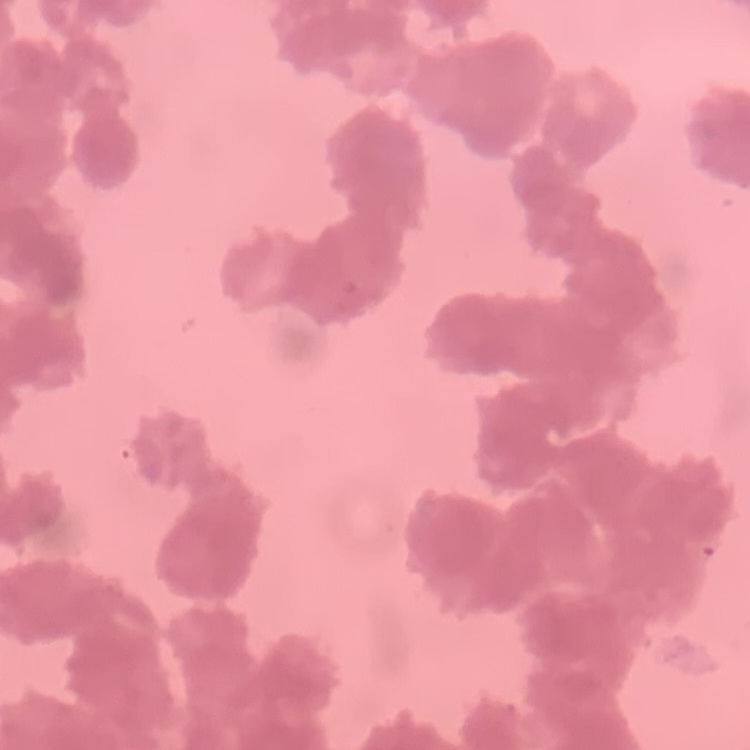

The erythrocytes exhibit rouleaux formation. Square crop of a larger photomicrograph. Stained with either Field's or Giemsa. Thin blood smear.